Name the parasite shown.
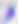

This is Toxoplasma gondii.

magnification = 400x
modality = micrograph